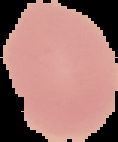
Summary:
  - Image size: 118×142 pixels
  - Malaria status: uninfected
  - Image type: cell region segmented out of the field of view; surrounding area masked to black
  - Preparation: thin blood film